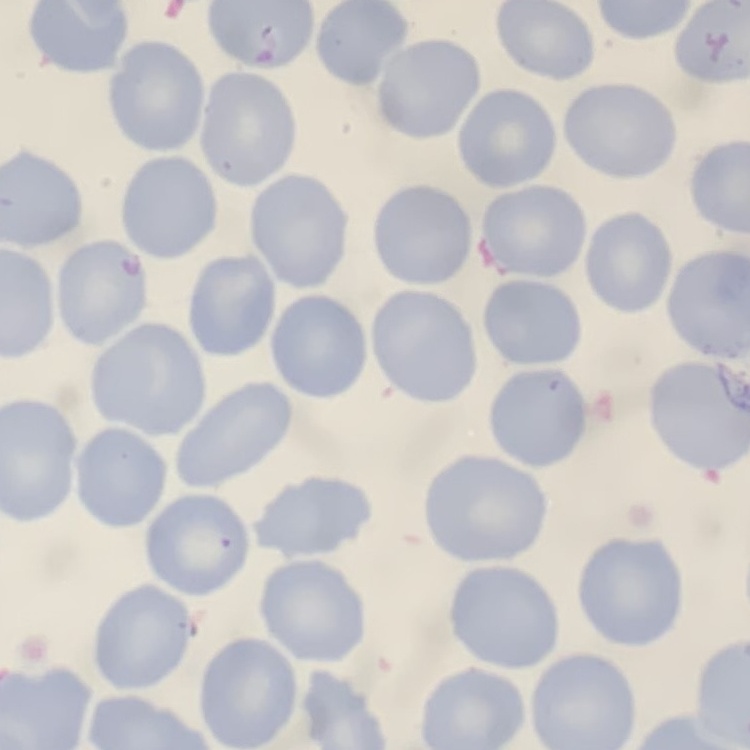
Summary:
  - Red blood cell morphology: no rouleaux formation
  - Stain: Field's or Giemsa
  - Preparation: thin peripheral smear
  - Image type: one tile cut from a larger photomicrograph